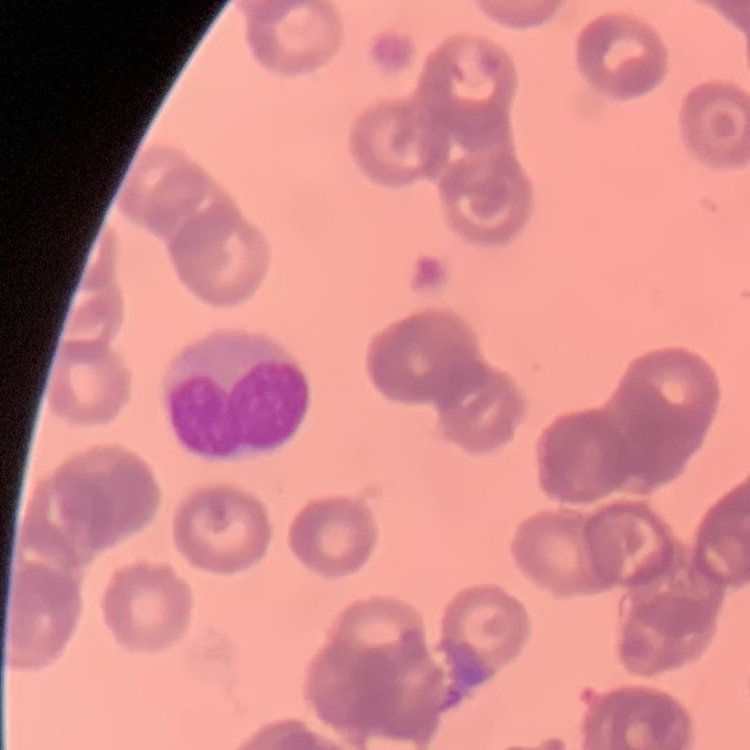

Summary:
  - Red blood cell morphology: rouleaux formation
  - Preparation: thin peripheral smear
  - Stain: Field's or Giemsa
  - Image type: one tile cut from a larger photomicrograph